Outline each uninfected red blood cell.
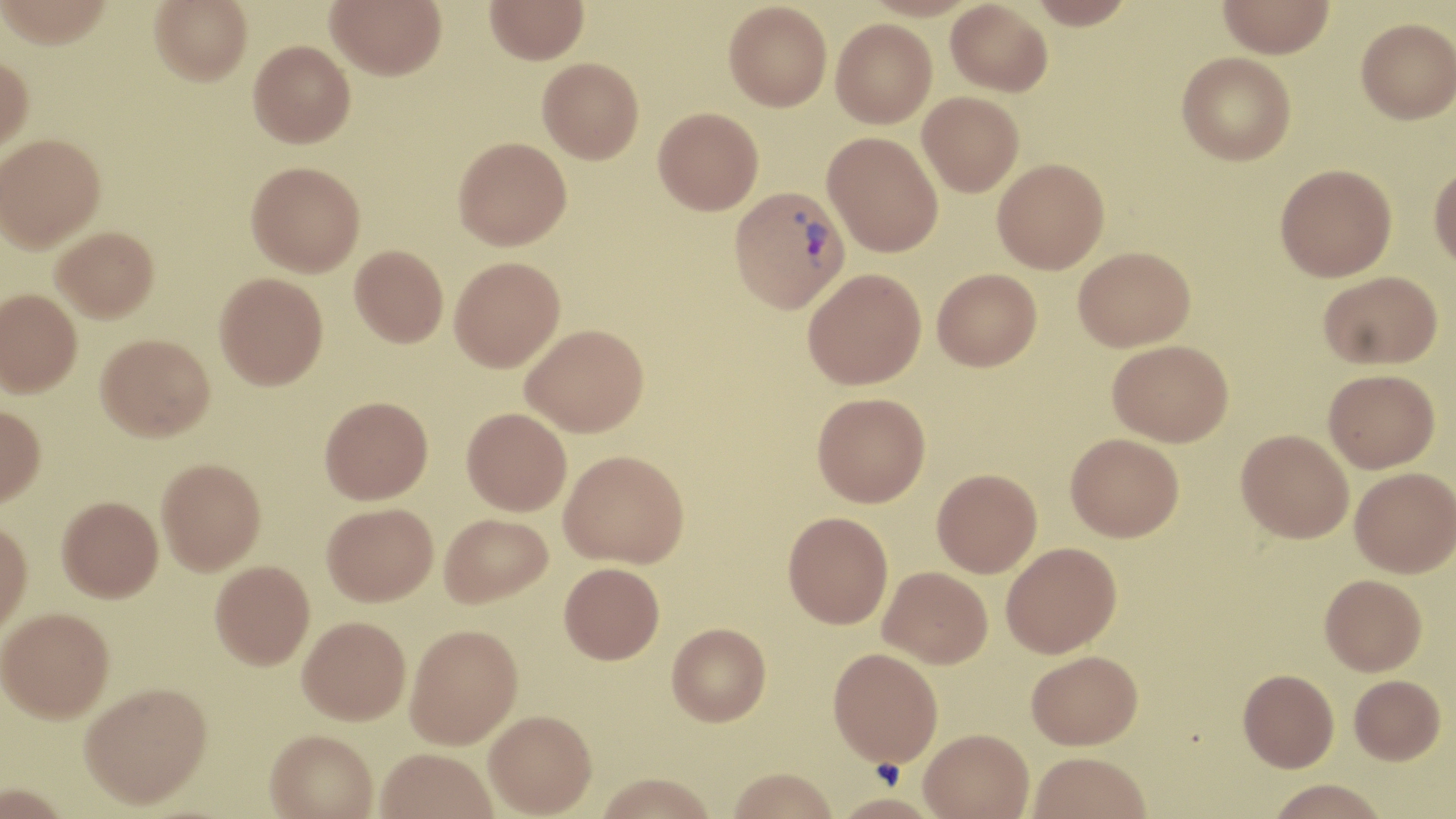
Approximate bounding boxes as named x1/y1/x2/y2 corners in pixels.
Uninfected red blood cells: (x1=0, y1=0, x2=114, y2=48), (x1=150, y1=0, x2=252, y2=85), (x1=326, y1=0, x2=446, y2=80), (x1=485, y1=0, x2=589, y2=64), (x1=1027, y1=0, x2=1136, y2=28), (x1=1217, y1=0, x2=1334, y2=58), (x1=723, y1=1, x2=832, y2=111), (x1=946, y1=1, x2=1052, y2=97), (x1=1356, y1=17, x2=1455, y2=123), (x1=831, y1=18, x2=937, y2=128), (x1=248, y1=40, x2=355, y2=148), (x1=1177, y1=52, x2=1296, y2=165), (x1=0, y1=53, x2=33, y2=153), (x1=537, y1=57, x2=643, y2=163), (x1=918, y1=91, x2=1024, y2=196), (x1=653, y1=107, x2=764, y2=215), (x1=823, y1=131, x2=944, y2=257), (x1=0, y1=133, x2=106, y2=251), (x1=453, y1=137, x2=571, y2=250), (x1=992, y1=158, x2=1109, y2=274), (x1=246, y1=161, x2=365, y2=276), (x1=1429, y1=162, x2=1456, y2=271), (x1=1275, y1=163, x2=1397, y2=281), (x1=52, y1=226, x2=159, y2=322), (x1=350, y1=244, x2=449, y2=347), (x1=1073, y1=246, x2=1195, y2=351), (x1=449, y1=256, x2=565, y2=371), (x1=803, y1=268, x2=926, y2=389), (x1=932, y1=268, x2=1042, y2=371), (x1=1318, y1=270, x2=1442, y2=369), (x1=215, y1=272, x2=328, y2=390), (x1=0, y1=289, x2=82, y2=396), (x1=521, y1=324, x2=649, y2=437), (x1=96, y1=333, x2=215, y2=441), (x1=1107, y1=339, x2=1233, y2=446), (x1=1323, y1=368, x2=1440, y2=472), (x1=812, y1=392, x2=930, y2=507), (x1=319, y1=395, x2=433, y2=504), (x1=0, y1=405, x2=46, y2=508), (x1=462, y1=407, x2=572, y2=516), (x1=1236, y1=429, x2=1354, y2=543), (x1=1065, y1=433, x2=1184, y2=541), (x1=559, y1=449, x2=688, y2=568), (x1=156, y1=457, x2=266, y2=575), (x1=1350, y1=467, x2=1455, y2=577), (x1=932, y1=468, x2=1042, y2=577), (x1=57, y1=495, x2=163, y2=602), (x1=322, y1=502, x2=438, y2=606), (x1=783, y1=511, x2=893, y2=629), (x1=439, y1=513, x2=552, y2=608), (x1=0, y1=519, x2=33, y2=637), (x1=1001, y1=542, x2=1121, y2=658), (x1=209, y1=560, x2=315, y2=669), (x1=559, y1=562, x2=665, y2=663), (x1=879, y1=566, x2=993, y2=668), (x1=1320, y1=574, x2=1427, y2=676), (x1=0, y1=608, x2=115, y2=725), (x1=298, y1=616, x2=411, y2=725), (x1=667, y1=622, x2=771, y2=725), (x1=406, y1=623, x2=523, y2=749), (x1=828, y1=647, x2=943, y2=766), (x1=1026, y1=650, x2=1142, y2=749), (x1=1238, y1=669, x2=1339, y2=771), (x1=1349, y1=675, x2=1445, y2=764), (x1=80, y1=685, x2=213, y2=813), (x1=484, y1=709, x2=596, y2=817), (x1=919, y1=728, x2=1033, y2=819), (x1=265, y1=731, x2=377, y2=818), (x1=376, y1=749, x2=498, y2=819), (x1=1028, y1=751, x2=1152, y2=819), (x1=726, y1=767, x2=838, y2=819), (x1=594, y1=772, x2=720, y2=819), (x1=1265, y1=780, x2=1390, y2=819).

Platelet locations: (x1=871, y1=758, x2=906, y2=790). Plasmodium vivax-infected red blood cell locations: (x1=729, y1=185, x2=850, y2=314). Slide-level diagnosis: Plasmodium vivax. Light microscopy. 1000x magnification. Single field of view. Image is 1456×819 pixels. May-Grünwald-Giemsa-stained preparation. Thin blood smear.